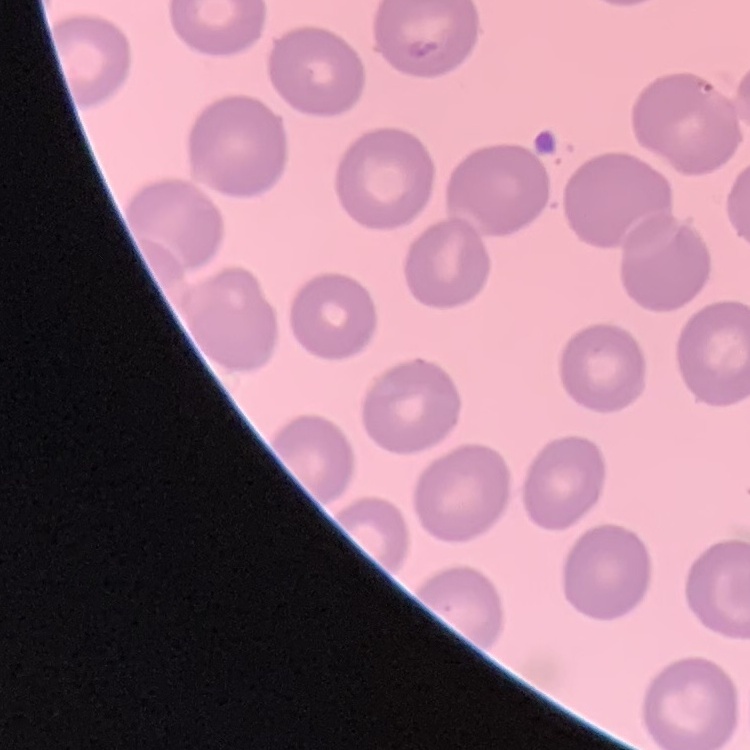
The red blood cells exhibit no rouleaux formation. Thin blood smear. Square crop of a larger photomicrograph. Field's or Giemsa stain.